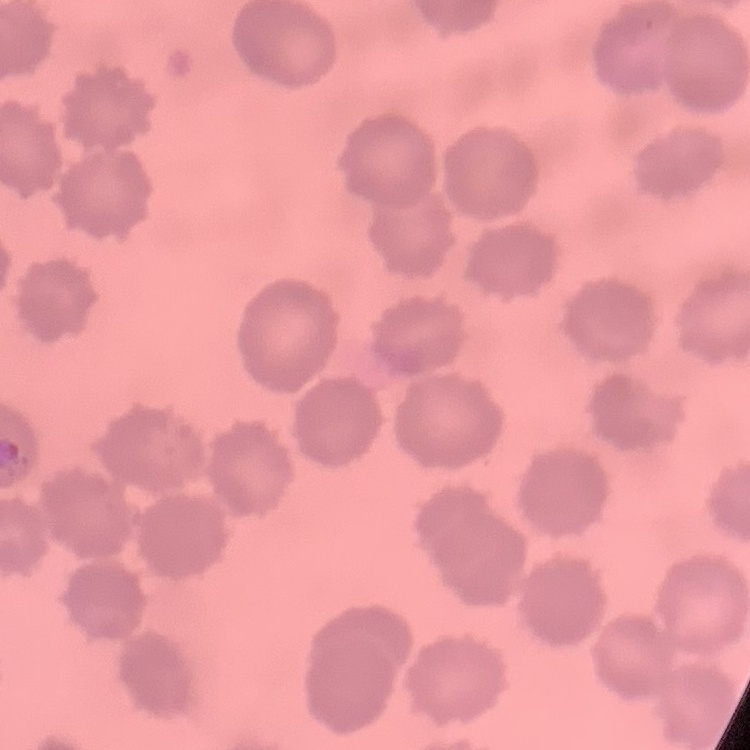
erythrocyte morphology = no rouleaux formation
image type = square crop of a larger photomicrograph
stain = Field's or Giemsa
preparation = thin blood film